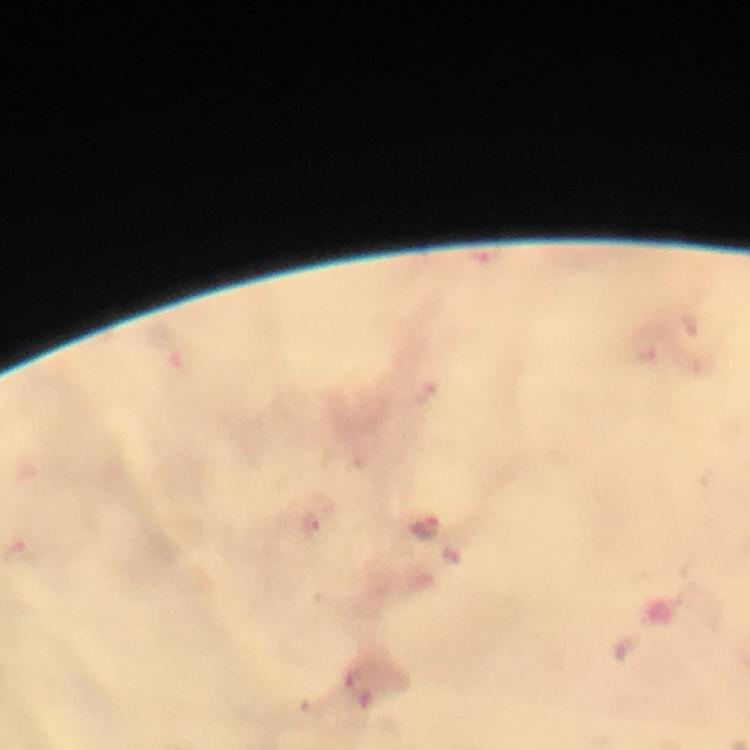
Approximate centers as (x, y) in pixels.
Summary:
  - Malaria parasite locations: (488, 257), (424, 529)
  - Image size: 750×750 pixels
  - Context: from a malaria diagnostic workup
  - Stain: Giemsa
  - Immersion oil: applied
  - Cropped from: one field of view
  - Capture: smartphone mounted on the microscope
  - Magnification: 100x
  - Preparation: thick blood smear